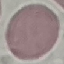

Result: no malaria parasites seen. Acquired by smartphone through the microscope eyepiece. Thin blood film. Giemsa stain. Cell patch, automatically extracted from a larger field of view and resized to 64 × 64 pixels.